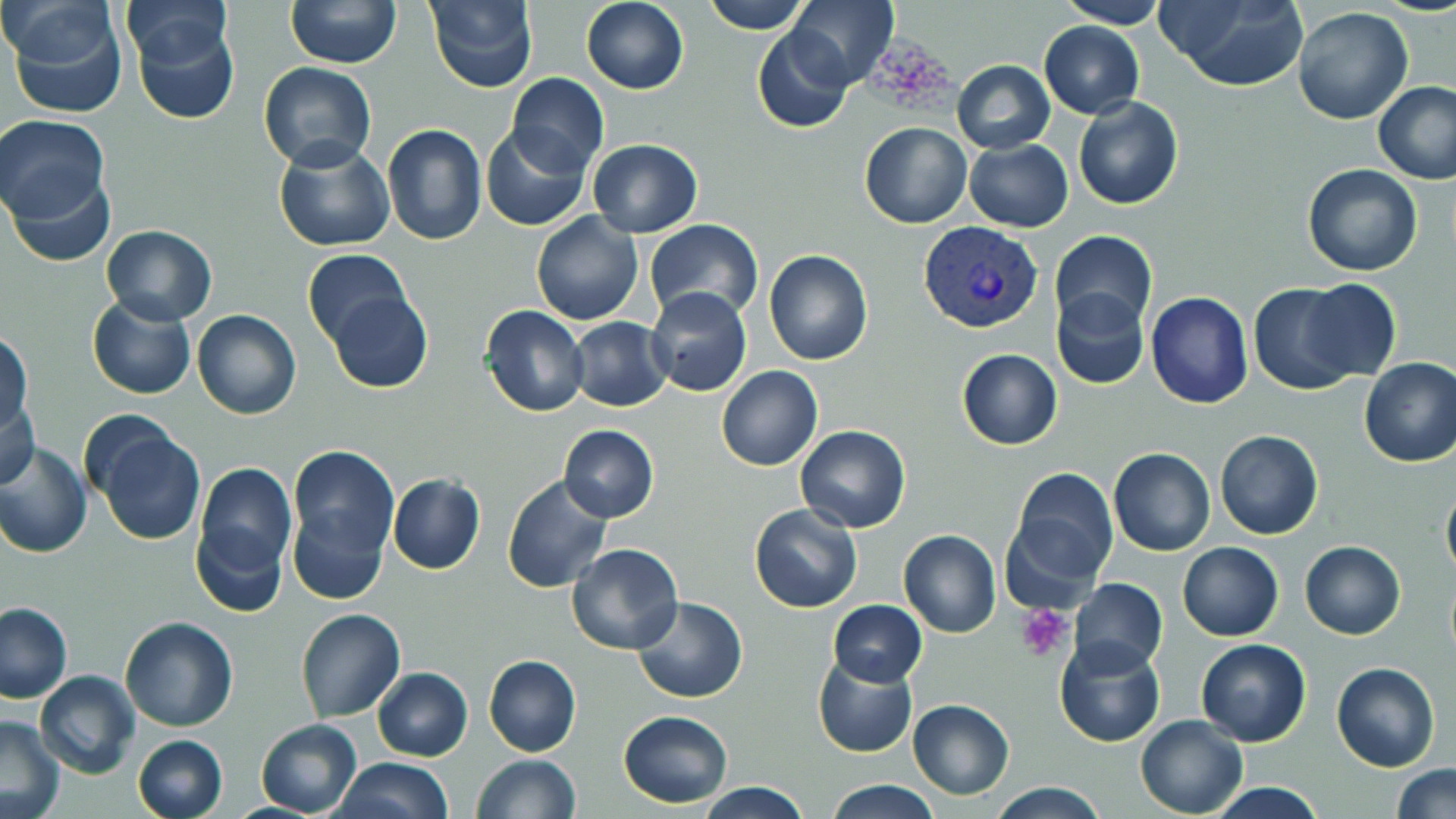

slide-level diagnosis = Plasmodium vivax
preparation = thin blood film
platelet locations = approximate bounding boxes as (x1,y1)-(x2,y2) corner pairs in pixels: (1018,605)-(1073,662)
magnification = 1000x
modality = light microscopy
stain = May-Grünwald-Giemsa
Plasmodium vivax-infected red blood cell locations = approximate bounding boxes as (x1,y1)-(x2,y2) corner pairs in pixels: (919,221)-(1042,335)
field of view = one of a larger specimen
uninfected red blood cell locations = approximate bounding boxes as (x1,y1)-(x2,y2) corner pairs in pixels: (121,0)-(232,72), (286,0)-(402,69), (425,0)-(538,91), (582,0)-(688,93), (704,0)-(810,33), (787,0)-(898,89), (1056,0)-(1166,29), (1157,0)-(1310,91), (5,2)-(129,120), (1293,8)-(1414,125), (130,14)-(239,125), (1039,20)-(1144,118), (752,28)-(854,131), (952,59)-(1056,153), (258,62)-(376,171), (506,73)-(608,176), (1373,82)-(1456,183), (1073,94)-(1184,210), (1,115)-(109,223), (860,122)-(971,228), (382,123)-(486,245), (480,127)-(589,230), (586,138)-(702,237), (274,140)-(395,252), (964,140)-(1073,232), (1302,164)-(1423,277), (4,170)-(116,270), (530,213)-(643,326), (644,219)-(762,327), (100,225)-(217,326), (1050,230)-(1157,332), (764,248)-(874,365), (301,250)-(413,348), (1295,280)-(1402,383), (1249,282)-(1367,396), (646,286)-(752,397), (1051,286)-(1149,388), (328,290)-(432,393), (1146,291)-(1252,409), (87,296)-(195,400), (482,305)-(588,417), (192,309)-(301,420), (567,316)-(672,412), (0,332)-(31,432), (956,349)-(1063,450), (1359,357)-(1456,468), (716,365)-(822,471), (1,397)-(41,490), (89,418)-(206,547), (558,424)-(659,524), (794,425)-(910,532), (1215,430)-(1324,540), (0,439)-(93,558), (288,445)-(399,560), (1109,447)-(1215,556), (194,463)-(297,581), (1006,467)-(1119,591), (387,474)-(486,574), (502,475)-(612,592), (1441,478)-(1456,587), (749,505)-(862,614), (289,507)-(387,605), (191,519)-(291,619), (899,530)-(1001,639), (1299,540)-(1405,640), (566,541)-(684,655), (1177,541)-(1284,642), (1067,578)-(1168,673), (632,596)-(747,704), (828,600)-(927,686), (0,601)-(72,703), (295,608)-(406,723), (119,618)-(237,732), (1054,633)-(1167,747), (1195,637)-(1312,747), (484,654)-(581,759), (812,656)-(918,758), (1331,662)-(1440,770), (373,667)-(473,760), (34,669)-(139,779), (907,699)-(1014,799), (618,710)-(734,808), (1135,714)-(1248,818), (0,715)-(65,818), (255,719)-(363,817), (132,735)-(227,819), (474,755)-(580,819), (332,758)-(453,817), (1390,765)-(1455,818), (824,779)-(944,818), (1204,780)-(1328,818), (694,781)-(810,819), (988,782)-(1109,818)
image size = 1456×819 pixels